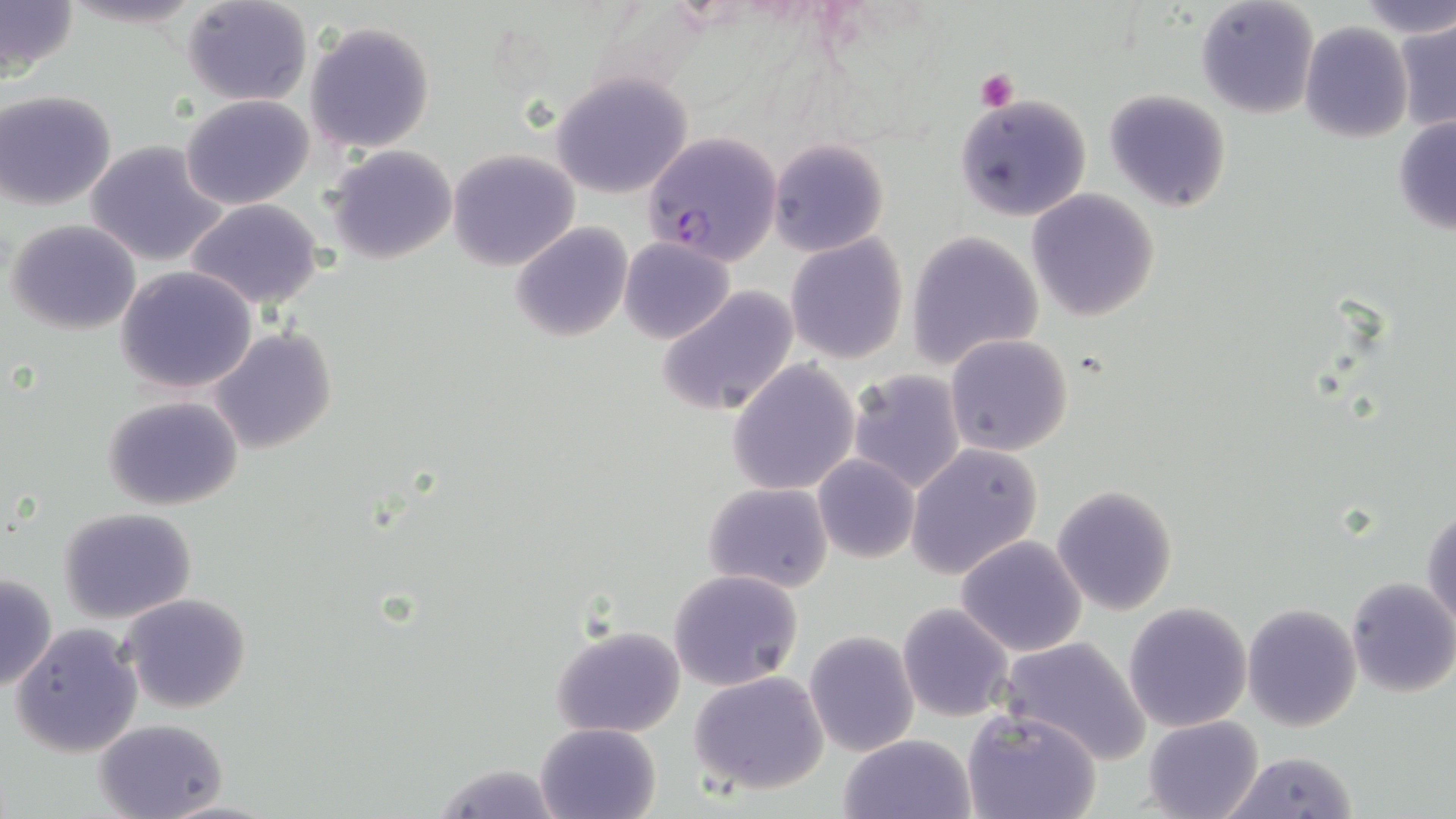 Approximate bounding boxes as [x1, y1, x2, y2] in pixels. Plasmodium falciparum-infected red blood cell locations: [643, 130, 783, 266]. Uninfected red blood cell locations: [0, 0, 79, 82], [180, 0, 314, 107], [1350, 0, 1454, 37], [1196, 1, 1318, 119], [1395, 16, 1456, 134], [306, 20, 435, 153], [1299, 22, 1414, 144], [550, 71, 694, 197], [1104, 88, 1232, 212], [1, 91, 117, 211], [956, 94, 1092, 221], [180, 95, 314, 209], [1391, 115, 1456, 236], [83, 139, 230, 268], [769, 139, 889, 257], [326, 145, 456, 263], [447, 148, 581, 270], [1026, 189, 1162, 322], [184, 198, 328, 310], [5, 218, 141, 334], [510, 222, 632, 342], [907, 231, 1044, 369], [784, 234, 908, 364], [619, 236, 735, 345], [115, 265, 260, 394], [658, 284, 800, 417], [209, 327, 338, 456], [944, 334, 1074, 458], [726, 360, 861, 495], [847, 368, 967, 494], [103, 395, 243, 511], [907, 443, 1042, 580], [812, 455, 920, 563], [704, 482, 834, 594], [1052, 485, 1179, 616], [1422, 503, 1455, 631], [59, 507, 198, 623], [956, 535, 1088, 657], [668, 568, 803, 691], [0, 573, 56, 691], [1345, 576, 1456, 697], [119, 594, 253, 715], [1123, 601, 1252, 731], [897, 602, 1015, 721], [1242, 602, 1362, 732], [9, 622, 143, 758], [551, 624, 687, 739], [804, 631, 920, 756], [999, 636, 1150, 764], [689, 672, 828, 795], [963, 708, 1101, 819], [1144, 716, 1264, 819], [95, 717, 228, 819], [535, 722, 660, 819], [836, 734, 977, 819], [1222, 751, 1360, 819], [157, 798, 280, 818]. Platelet locations: [973, 69, 1018, 111]. Slide-level diagnosis: Plasmodium falciparum. May-Grünwald-Giemsa stain. Optical microscopy. Thin blood smear. Captured at 1000x magnification. Image is 1456×819 pixels. One field of a larger specimen.